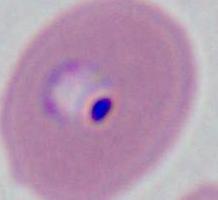

A Plasmodium parasite is seen. Captured at either 400x or 1000x magnification. Micrograph.